State which parasite is depicted.
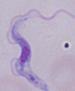

A trypanosome.

Micrograph. Captured at 1000x magnification.